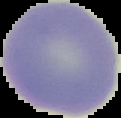 Result: no malaria parasites detected. Image is 121×118 pixels. Cell region segmented out of the field of view; the surrounding area is masked to black. From a thin blood film.